Report the malaria status of this cell.
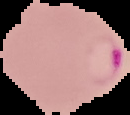
It is parasitized.

{
  "image_type": "segmented cell region on a black background",
  "image_size": "130×115 pixels",
  "preparation": "thin blood film"
}